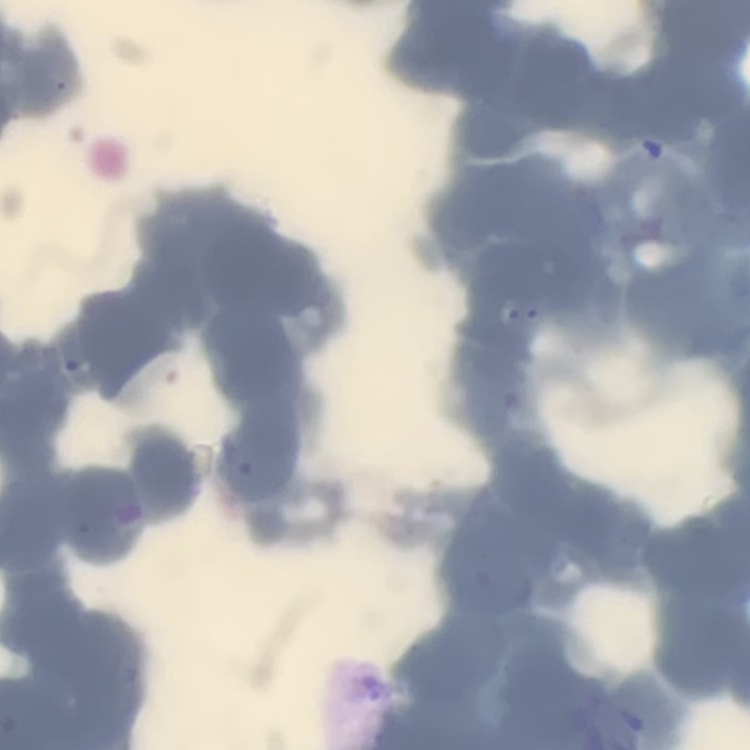
The erythrocytes show rouleaux formation. Square crop of a larger photomicrograph. Stained with either Field's or Giemsa. Thin blood smear.